Identify the parasite.
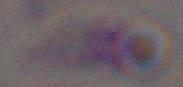

Toxoplasma gondii.

modality = micrograph
magnification = 1000x